State which cell type is depicted.
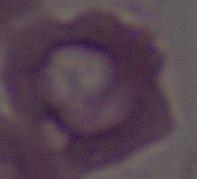

This is an erythrocyte.

Micrograph. 1000x magnification.